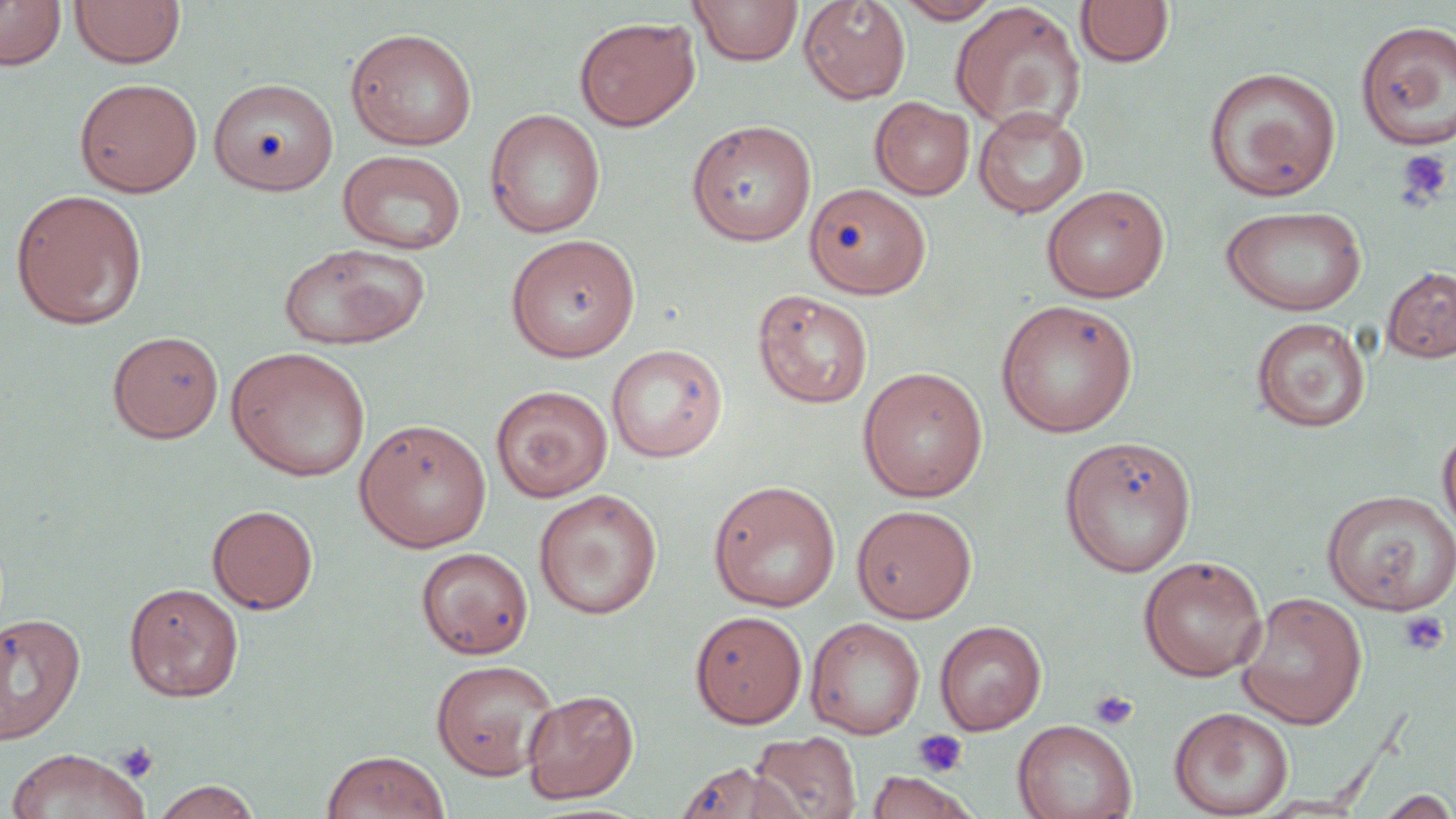
slide_level_diagnosis: negative for blood parasites
platelet_locations: 'approximate bounding boxes as (x1, y1, x2, y2) in pixels: (1395, 148, 1454, 209), (1398, 611, 1450, 655), (1089, 689, 1138, 731), (912, 729, 968, 777), (116, 741, 158, 782)'
field_of_view: single
image_size: 1456×819 pixels
preparation: thin blood film
stain: May-Grünwald-Giemsa
magnification: 1000x
uninfected_red_blood_cell_locations: 'approximate bounding boxes as (x1, y1, x2, y2) in pixels: (0, 0, 66, 71), (69, 0, 186, 69), (690, 0, 803, 66), (798, 0, 911, 104), (894, 0, 1004, 24), (1076, 0, 1173, 68), (950, 2, 1086, 133), (574, 16, 700, 131), (1355, 19, 1456, 150), (345, 27, 478, 151), (1205, 66, 1341, 201), (74, 78, 203, 198), (208, 78, 338, 196), (870, 97, 974, 200), (973, 106, 1090, 218), (485, 108, 606, 238), (686, 119, 817, 246), (337, 149, 466, 255), (805, 182, 931, 298), (1041, 184, 1170, 303), (9, 188, 149, 330), (1219, 205, 1368, 316), (506, 234, 641, 362), (276, 242, 432, 351), (1383, 266, 1456, 363), (752, 289, 873, 409), (996, 299, 1139, 438), (1250, 318, 1371, 432), (107, 330, 225, 443), (606, 343, 728, 462), (225, 346, 371, 482), (857, 366, 989, 502), (490, 384, 613, 502), (354, 418, 492, 552), (1437, 422, 1456, 540), (1059, 436, 1197, 577), (708, 480, 841, 612), (1322, 488, 1455, 614), (533, 489, 662, 619), (851, 503, 977, 623), (206, 504, 319, 614), (416, 547, 534, 660), (1138, 555, 1267, 682), (124, 582, 245, 702), (1236, 591, 1367, 729), (689, 610, 807, 728), (0, 612, 85, 745), (806, 618, 926, 739), (934, 620, 1047, 735), (430, 659, 560, 780), (521, 689, 639, 804), (1169, 706, 1294, 818), (1013, 719, 1138, 819), (749, 730, 862, 819), (5, 747, 151, 819), (322, 749, 449, 819), (674, 761, 804, 819), (864, 771, 977, 818), (150, 779, 263, 819), (1373, 790, 1456, 818)'
modality: light microscopy